Report the malaria status of this cell.
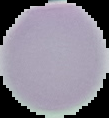

It is uninfected.

image_size: 109×118 pixels
image_type: cell region segmented out of the field of view; surrounding area masked to black
preparation: thin blood film